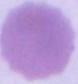
modality = micrograph
magnification = 1000x
identification = red blood cell